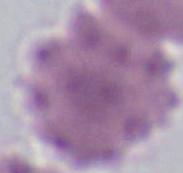
1000x magnification. An erythrocyte is shown. Micrograph.